Classify this cell by malaria status.
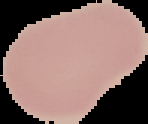

Uninfected.

Segmented cell region on a black background. Image is 148×124 pixels. From a thin blood smear.